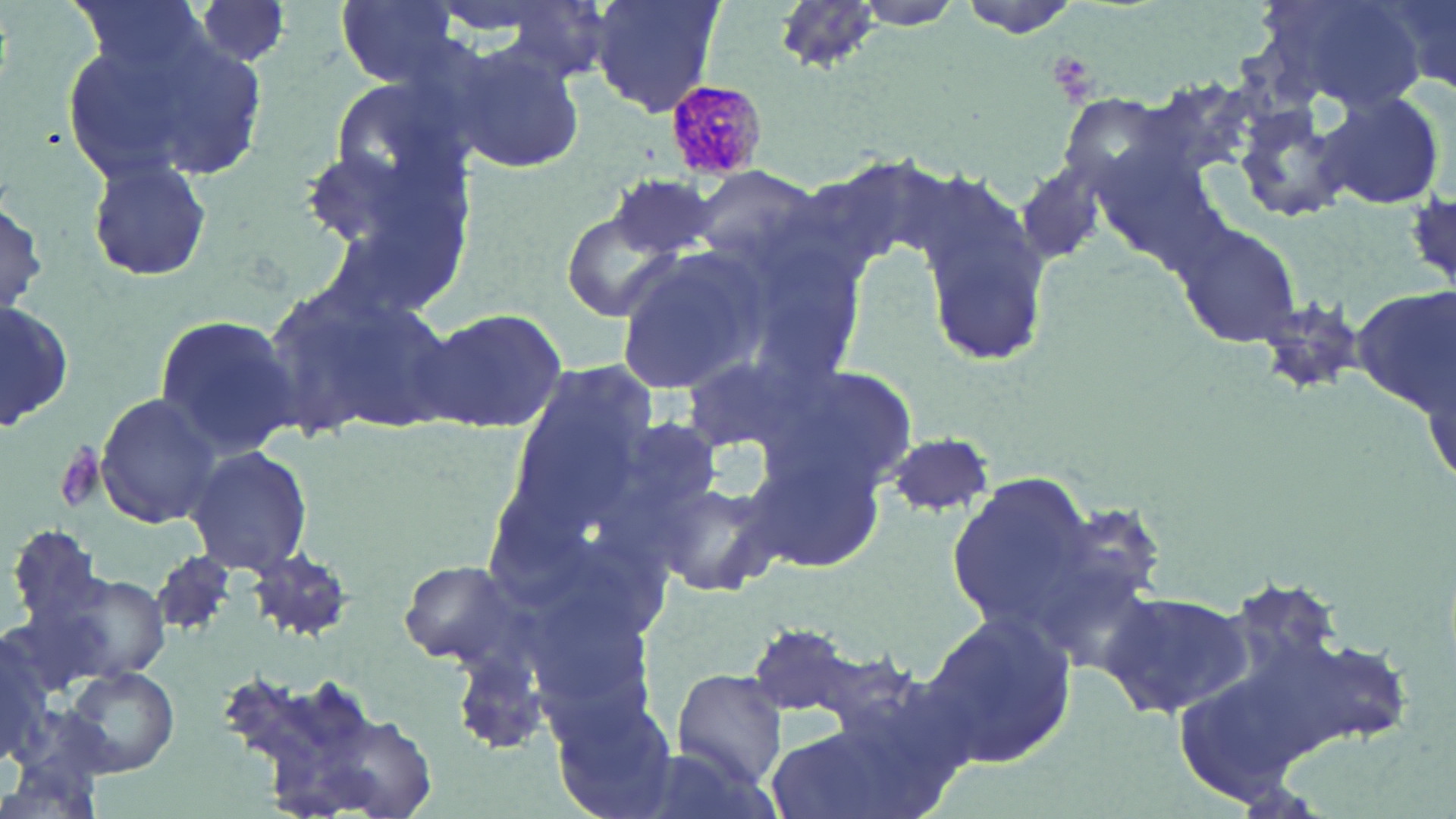
slide-level diagnosis = Plasmodium malariae
modality = optical microscopy
image size = 1456×819 pixels
stain = May-Grünwald-Giemsa
uninfected red blood cell locations = approximate bounding boxes as (x1,y1)-(x2,y2) corner pairs in pixels: (65,0)-(211,75), (191,0)-(296,69), (589,0)-(725,120), (953,0)-(1085,36), (1250,0)-(1431,110), (1369,0)-(1456,100), (333,1)-(464,86), (773,1)-(875,71), (124,33)-(276,184), (450,42)-(588,175), (1315,92)-(1447,212), (1237,105)-(1356,223), (296,132)-(473,305), (84,154)-(214,284), (686,166)-(825,273), (608,171)-(719,262), (912,175)-(1055,370), (1,193)-(47,321), (559,206)-(692,323), (1173,221)-(1302,347), (722,228)-(869,390), (615,248)-(768,394), (256,279)-(447,442), (1354,286)-(1455,416), (1,297)-(75,436), (413,306)-(570,430), (152,312)-(300,458), (762,357)-(926,502), (94,390)-(224,531), (883,432)-(996,516), (182,445)-(313,574), (744,451)-(886,573), (946,470)-(1098,636), (650,477)-(782,600), (6,521)-(112,638), (246,550)-(359,642), (151,551)-(240,641), (396,559)-(530,668), (53,572)-(174,683), (1101,589)-(1249,720), (919,610)-(1077,770), (742,621)-(882,724), (0,634)-(56,768), (215,659)-(396,816), (63,665)-(180,778), (674,670)-(789,786), (545,685)-(683,816), (760,714)-(945,819)
Plasmodium malariae-infected red blood cell locations = approximate bounding boxes as (x1,y1)-(x2,y2) corner pairs in pixels: (660,78)-(767,180)
preparation = thin blood smear
field of view = one of a larger specimen
magnification = 1000x